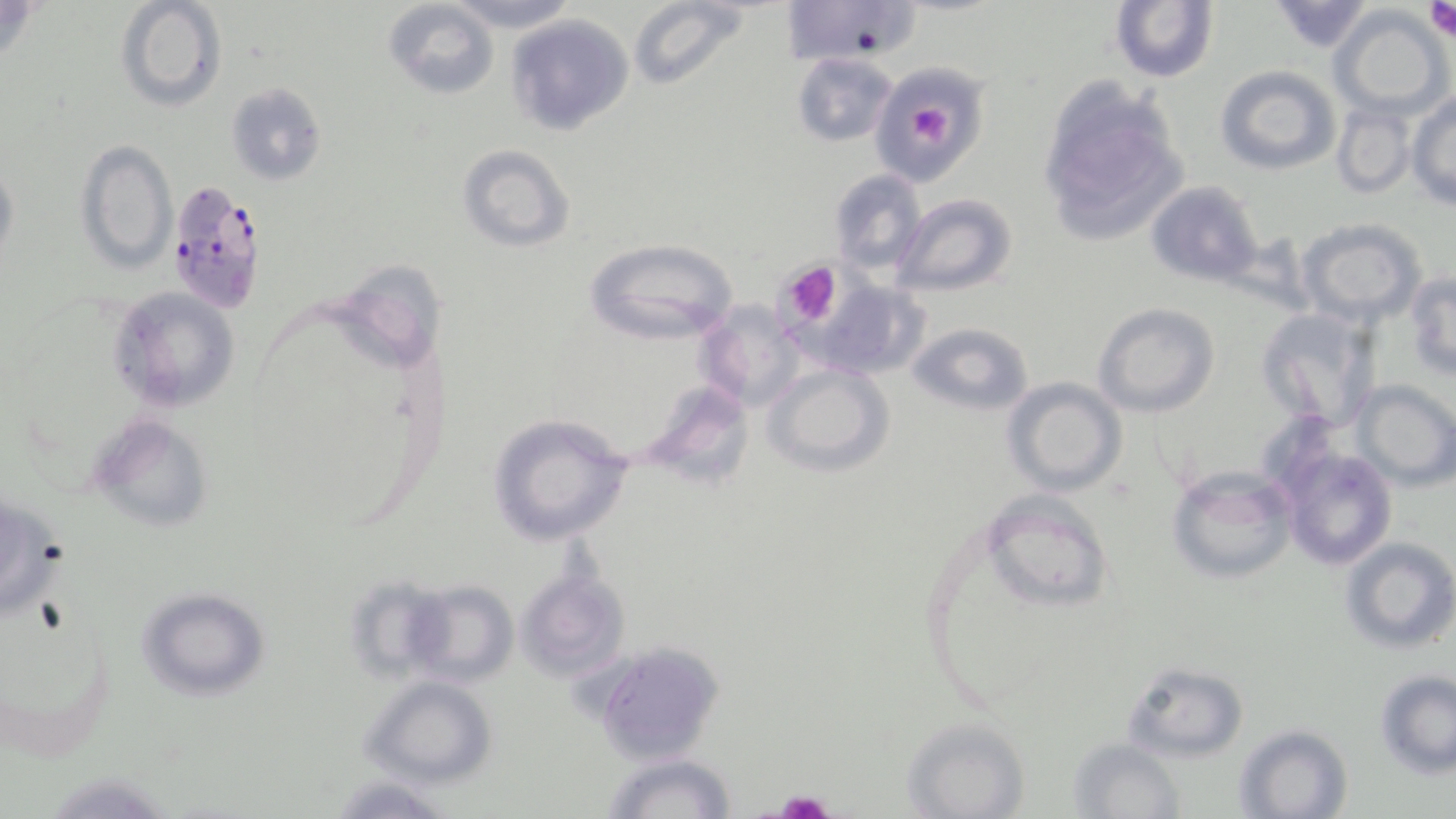

Summary:
  - Coordinate format: approximate bounding boxes as (x1, y1, x2, y2) in pixels
  - Platelet locations: (910, 102, 953, 138), (778, 260, 844, 329), (775, 791, 834, 819)
  - Plasmodium falciparum-infected red blood cell locations: (166, 183, 265, 315)
  - Uninfected red blood cell locations: (115, 0, 226, 112), (382, 0, 500, 100), (447, 0, 579, 33), (629, 0, 750, 91), (780, 0, 915, 66), (1110, 0, 1217, 84), (1265, 1, 1376, 53), (1331, 7, 1452, 115), (507, 15, 633, 136), (793, 56, 899, 150), (1214, 64, 1341, 175), (882, 67, 992, 192), (1035, 81, 1192, 244), (226, 83, 325, 184), (1407, 94, 1456, 210), (1331, 99, 1417, 198), (75, 138, 177, 277), (455, 144, 576, 252), (1, 161, 19, 266), (830, 169, 927, 275), (1144, 180, 1265, 286), (894, 194, 1018, 297), (1297, 218, 1426, 327), (582, 237, 742, 346), (332, 256, 452, 375), (1405, 272, 1456, 379), (815, 280, 933, 379), (106, 286, 240, 413), (696, 300, 805, 411), (1095, 304, 1220, 417), (1255, 307, 1378, 433), (908, 322, 1032, 417), (761, 363, 895, 476), (1002, 377, 1128, 497), (1351, 379, 1456, 490), (638, 380, 754, 487), (1304, 398, 1452, 553), (88, 413, 215, 535), (487, 413, 636, 546), (1278, 447, 1396, 572), (1166, 464, 1297, 584), (977, 490, 1113, 614), (1341, 537, 1456, 654), (516, 568, 632, 683), (344, 575, 456, 681), (405, 581, 518, 688), (137, 586, 271, 700), (0, 587, 117, 764), (590, 641, 727, 765), (1121, 662, 1248, 762), (1375, 670, 1456, 777), (359, 675, 499, 788), (901, 719, 1029, 818), (1235, 724, 1352, 818), (1068, 737, 1184, 818), (602, 752, 737, 819), (332, 774, 450, 817)
  - Slide-level diagnosis: Plasmodium falciparum
  - Preparation: thin blood smear
  - Modality: optical microscopy
  - Image size: 1456×819 pixels
  - Magnification: 1000x
  - Field of view: single
  - Stain: May-Grünwald-Giemsa